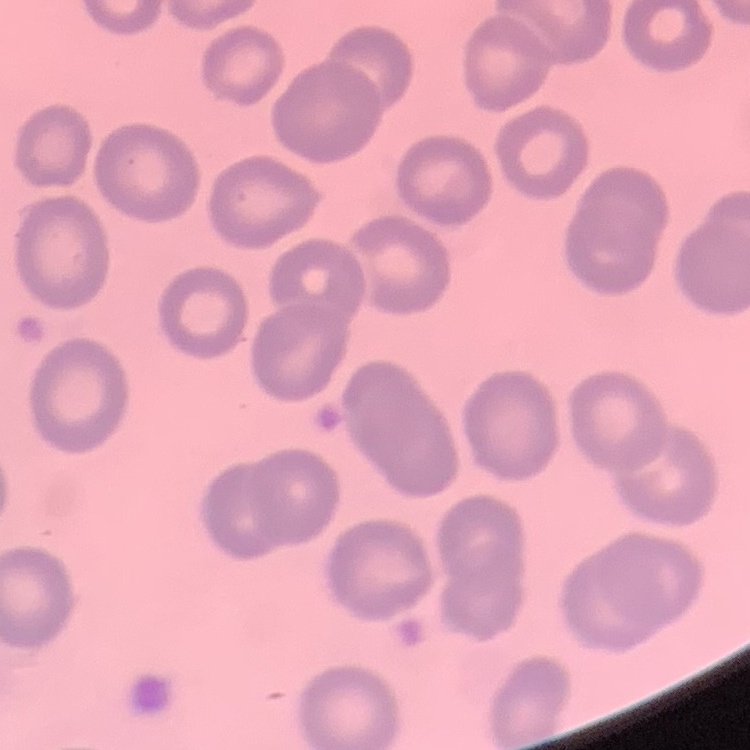
erythrocyte morphology = no rouleaux formation
image type = one tile cut from a larger photomicrograph
preparation = thin blood film
stain = Field's or Giemsa